Locate every Plasmodium parasite.
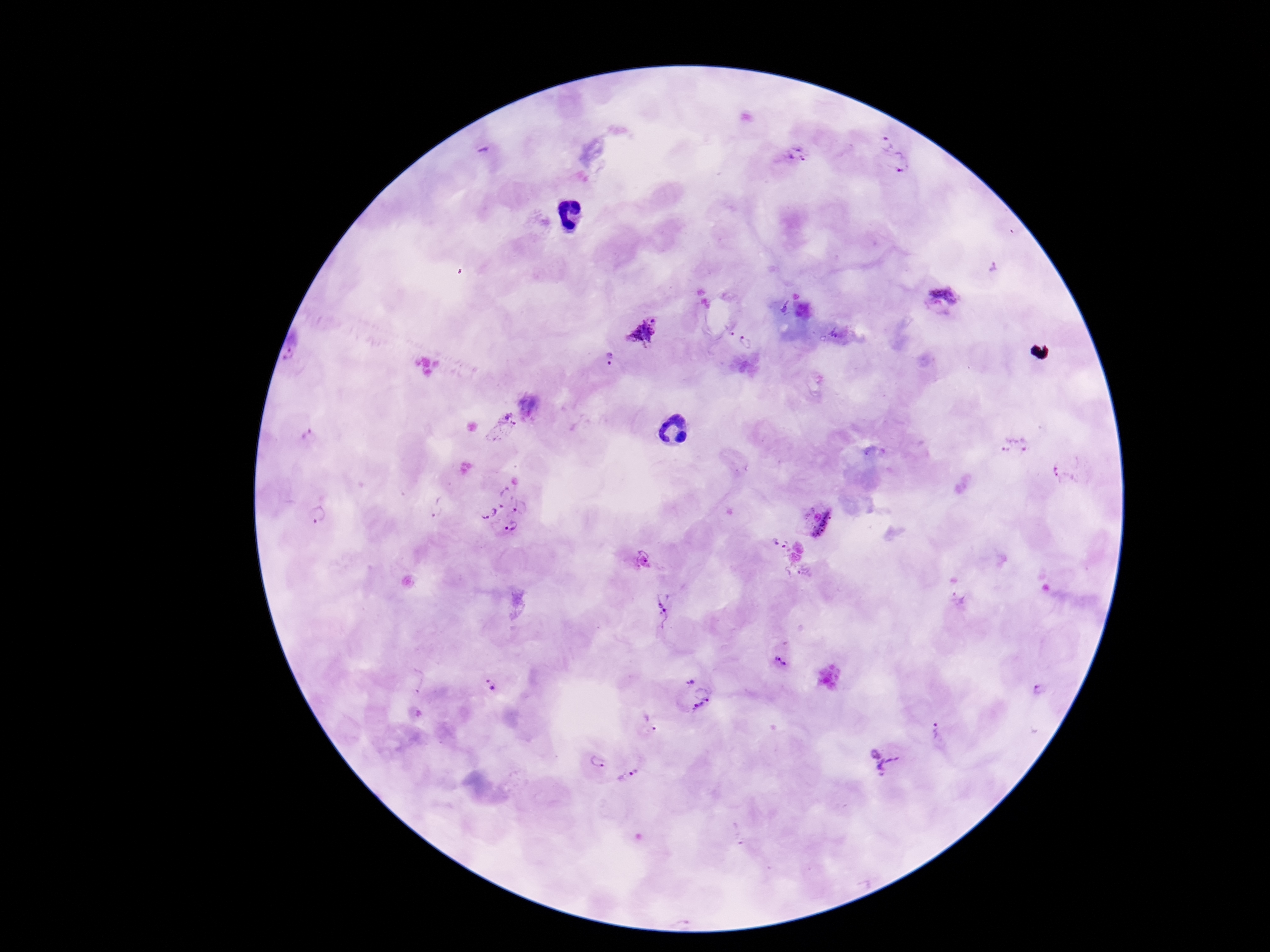
Approximate centers as (x, y) in pixels.
Plasmodium parasites: (884, 142), (485, 150), (797, 156), (900, 162), (993, 266), (948, 285), (936, 311), (729, 327), (833, 332), (643, 333), (747, 343), (609, 360), (502, 426), (308, 437), (1013, 446), (1066, 473), (437, 510), (504, 510), (319, 518), (818, 523), (780, 545), (643, 558), (662, 599), (959, 600), (662, 618), (783, 659), (690, 680), (417, 683), (491, 685), (1038, 691), (704, 694), (698, 707), (651, 723), (935, 730), (879, 758), (596, 762), (627, 774).

Single field of view. Patient malaria status: positive. Thick blood smear. Photographed through the microscope eyepiece with a smartphone camera. Giemsa-stained preparation. 100x magnification. Image is 1270×952 pixels.